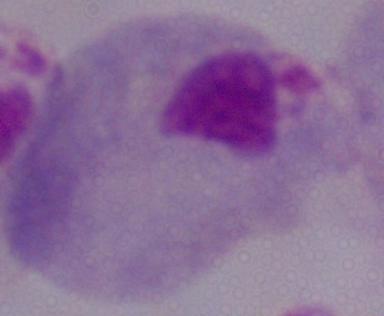 A trichomonad is seen. Captured at 1000x magnification. Micrograph.